Name the parasite shown.
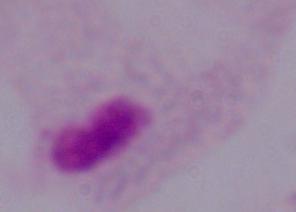
This is a trichomonad.

Summary:
  - Modality: photomicrograph
  - Magnification: 1000x